Assess this cell for malaria.
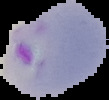
It is parasitized.

Cell region segmented out of the field of view; the surrounding area is masked to black. Image is 109×100 pixels. From a thin blood film.